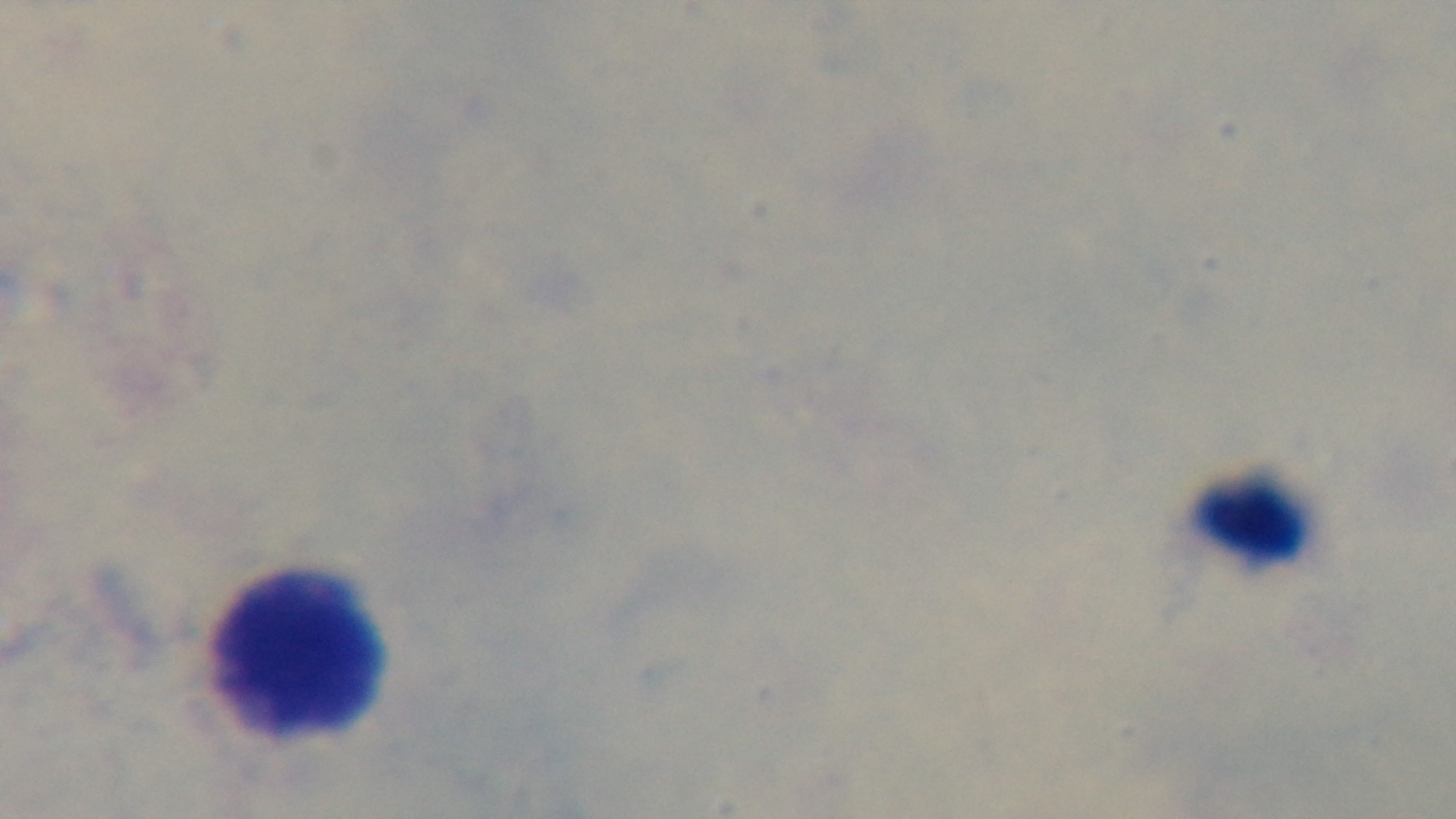

Summary:
  - Modality: light microscopy
  - Preparation: thick
  - Stain: Giemsa
  - Field of view: one from the slide
  - Objective: 100x oil immersion
  - Capture: mounted 4K digital camera
  - Malaria status: uninfected